Classify this cell by malaria status.
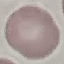
Uninfected.

Summary:
  - Image type: automatically extracted cell patch, resized to 64 × 64 pixels
  - Capture: smartphone through the microscope eyepiece
  - Preparation: thin blood film
  - Stain: Giemsa